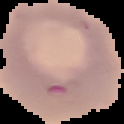
Summary:
  - Preparation: thin blood film
  - Result: no Plasmodium parasites seen
  - Image size: 124×124 pixels
  - Image type: cell region segmented out of the field of view; surrounding area masked to black